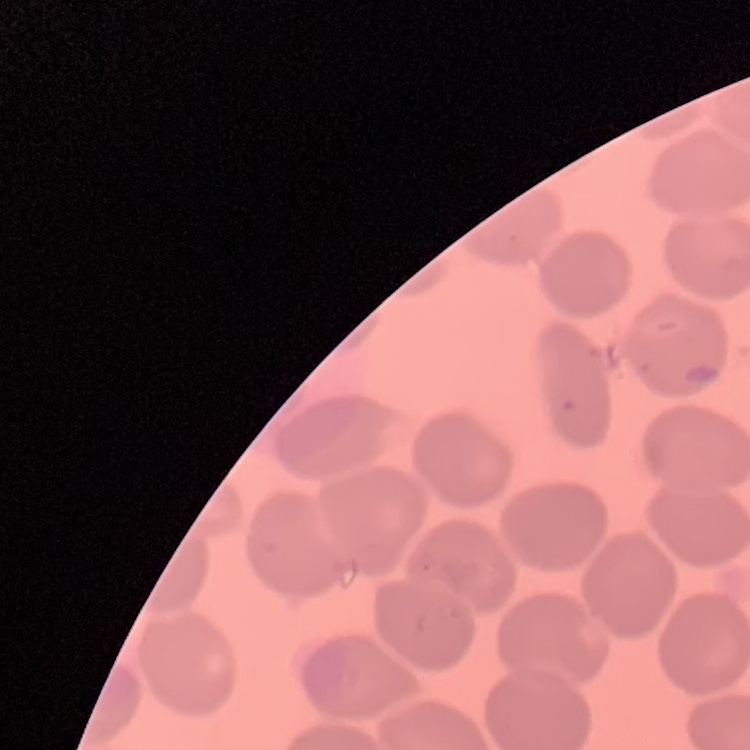

red_blood_cell_morphology: no rouleaux formation
image_type: square crop of a larger photomicrograph
preparation: thin blood film
stain: Field's or Giemsa